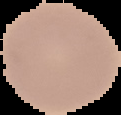

Summary:
  - Image size: 121×115 pixels
  - Image type: segmented cell region on a black background
  - Preparation: thin blood film
  - Result: no malaria parasites seen